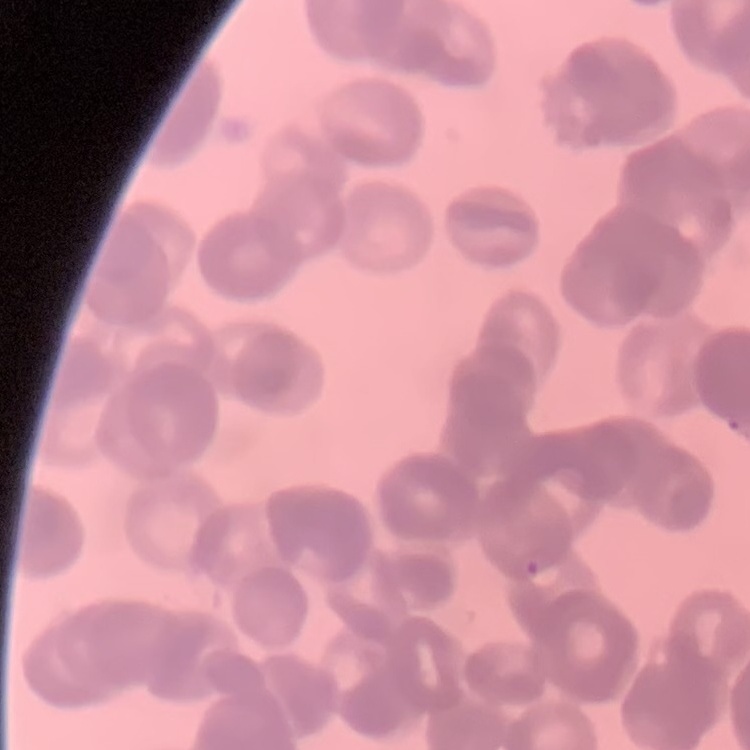
{
  "erythrocyte_morphology": "rouleaux formation",
  "image_type": "square crop of a larger photomicrograph",
  "preparation": "thin blood smear",
  "stain": "Field's or Giemsa"
}